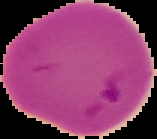

Segmented cell region on a black background. Result: malaria parasites detected. From a thin blood film. Image is 157×139 pixels.